Locate every Plasmodium falciparum-infected red blood cell.
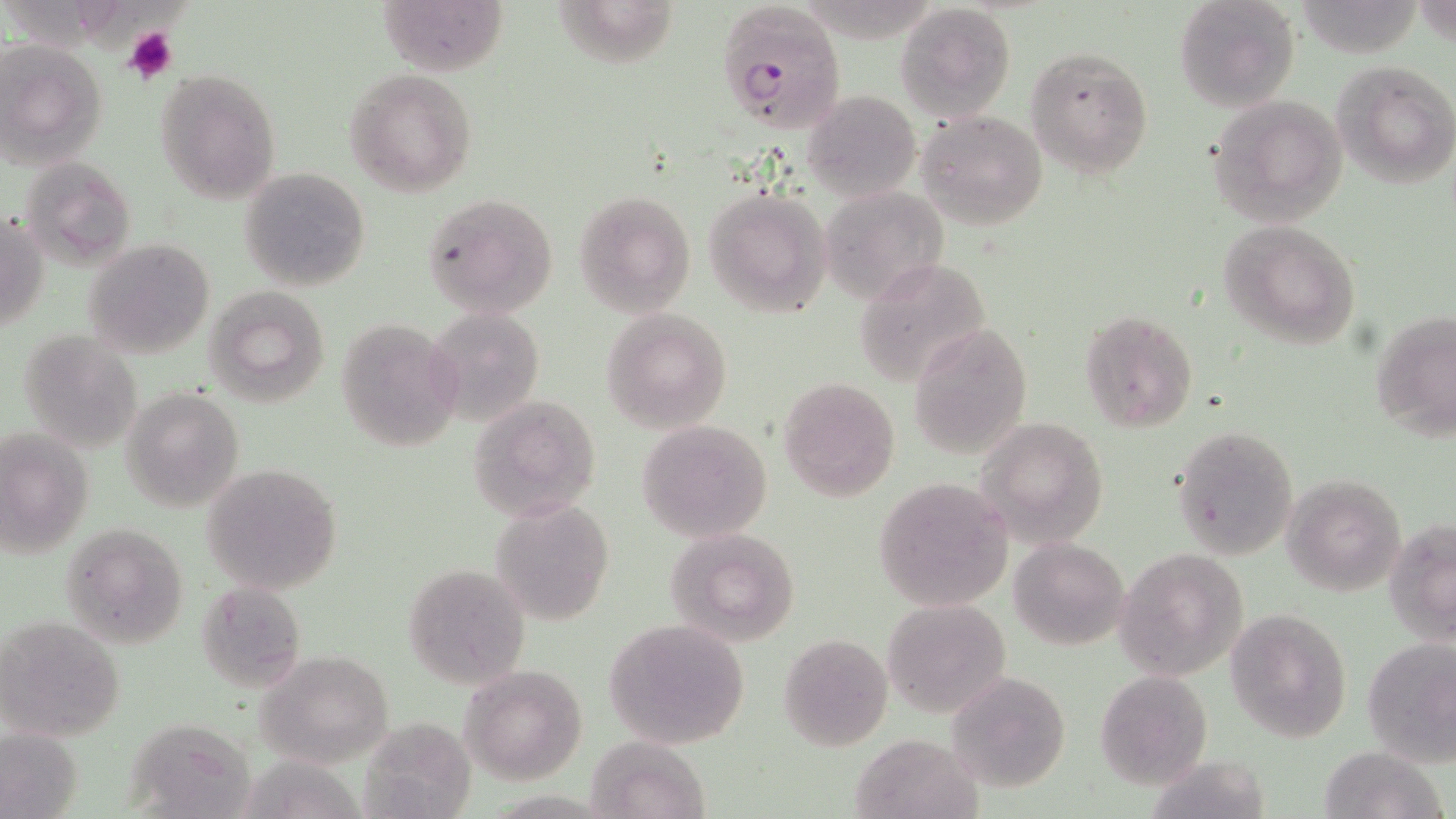

Approximate bounding boxes as [x1, y1, x2, y2] in pixels.
Plasmodium falciparum-infected red blood cells: [715, 0, 848, 132].

Summary:
  - Platelet locations: [122, 24, 179, 84]
  - Uninfected red blood cell locations: [1174, 0, 1302, 114], [379, 1, 508, 75], [547, 1, 678, 70], [896, 3, 1016, 122], [0, 39, 108, 169], [1023, 46, 1154, 179], [1332, 60, 1456, 188], [154, 69, 283, 203], [343, 69, 478, 196], [803, 89, 921, 201], [1208, 95, 1349, 227], [917, 109, 1049, 229], [20, 157, 137, 265], [239, 167, 371, 291], [819, 185, 949, 307], [704, 186, 834, 319], [575, 191, 696, 316], [424, 192, 559, 319], [1, 213, 49, 336], [1219, 220, 1360, 348], [83, 238, 216, 358], [854, 257, 993, 387], [203, 286, 331, 408], [427, 308, 545, 427], [601, 308, 732, 433], [1079, 308, 1197, 432], [1370, 308, 1454, 444], [334, 318, 463, 451], [907, 321, 1033, 459], [18, 329, 144, 454], [778, 376, 901, 502], [121, 388, 244, 511], [466, 395, 600, 520], [978, 418, 1110, 545], [636, 420, 772, 541], [1170, 425, 1299, 559], [0, 428, 95, 558], [202, 461, 344, 596], [1282, 474, 1406, 595], [873, 477, 1015, 612], [491, 499, 614, 625], [1385, 517, 1456, 645], [60, 521, 190, 648], [667, 526, 801, 646], [1010, 538, 1130, 650], [1115, 547, 1249, 679], [403, 564, 531, 689], [194, 580, 307, 693], [882, 597, 1012, 719], [1228, 608, 1352, 742], [0, 615, 125, 743], [604, 619, 751, 748], [776, 633, 893, 752], [1361, 637, 1456, 764], [255, 650, 394, 766], [461, 665, 587, 784], [1095, 670, 1212, 788], [945, 671, 1072, 792], [130, 715, 265, 819], [362, 716, 476, 818], [0, 724, 84, 819], [849, 731, 983, 819], [585, 736, 709, 819], [1316, 746, 1447, 819], [244, 751, 369, 819]
  - Slide-level diagnosis: Plasmodium falciparum
  - Stain: May-Grünwald-Giemsa
  - Image size: 1456×819 pixels
  - Magnification: 1000x
  - Modality: light microscopy
  - Field of view: single
  - Preparation: thin blood film